Classify this cell by malaria status.
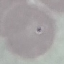
It is uninfected.

{
  "capture": "smartphone through the microscope eyepiece",
  "image_type": "cell patch, automatically extracted from a larger field of view and resized to 64 × 64 pixels",
  "stain": "Giemsa",
  "preparation": "thin blood smear"
}